Report the malaria status of this cell.
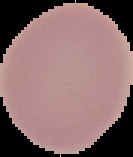

Uninfected.

From a thin blood smear. Segmented cell region on a black background. Image is 133×157 pixels.